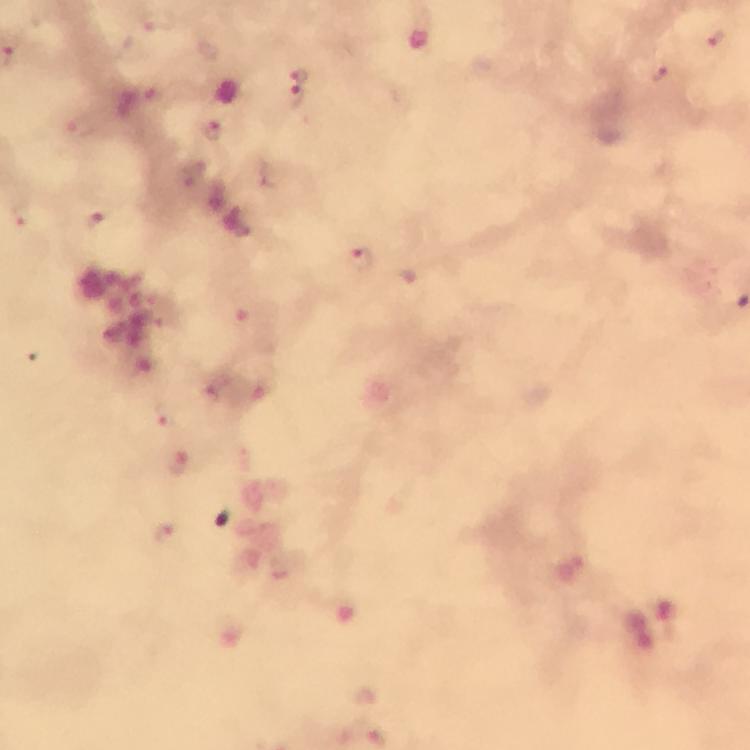

Approximate object centers, in pixels from the top-left corner.
Summary:
  - Malaria parasite locations: (x=156, y=21), (x=715, y=40), (x=660, y=73), (x=299, y=74), (x=296, y=97), (x=79, y=127), (x=17, y=217), (x=97, y=220), (x=360, y=258), (x=246, y=318), (x=163, y=416), (x=180, y=463), (x=164, y=532)
  - Capture: smartphone mounted on the microscope
  - Magnification: 100x
  - Image size: 750×750 pixels
  - Immersion oil: applied
  - Preparation: thick smear
  - Stain: Giemsa
  - Cropped from: a single field of view
  - Context: from a diagnostic examination for malaria